State which cell type is depicted.
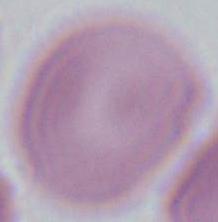

An erythrocyte.

Micrograph. Captured at 1000x magnification.